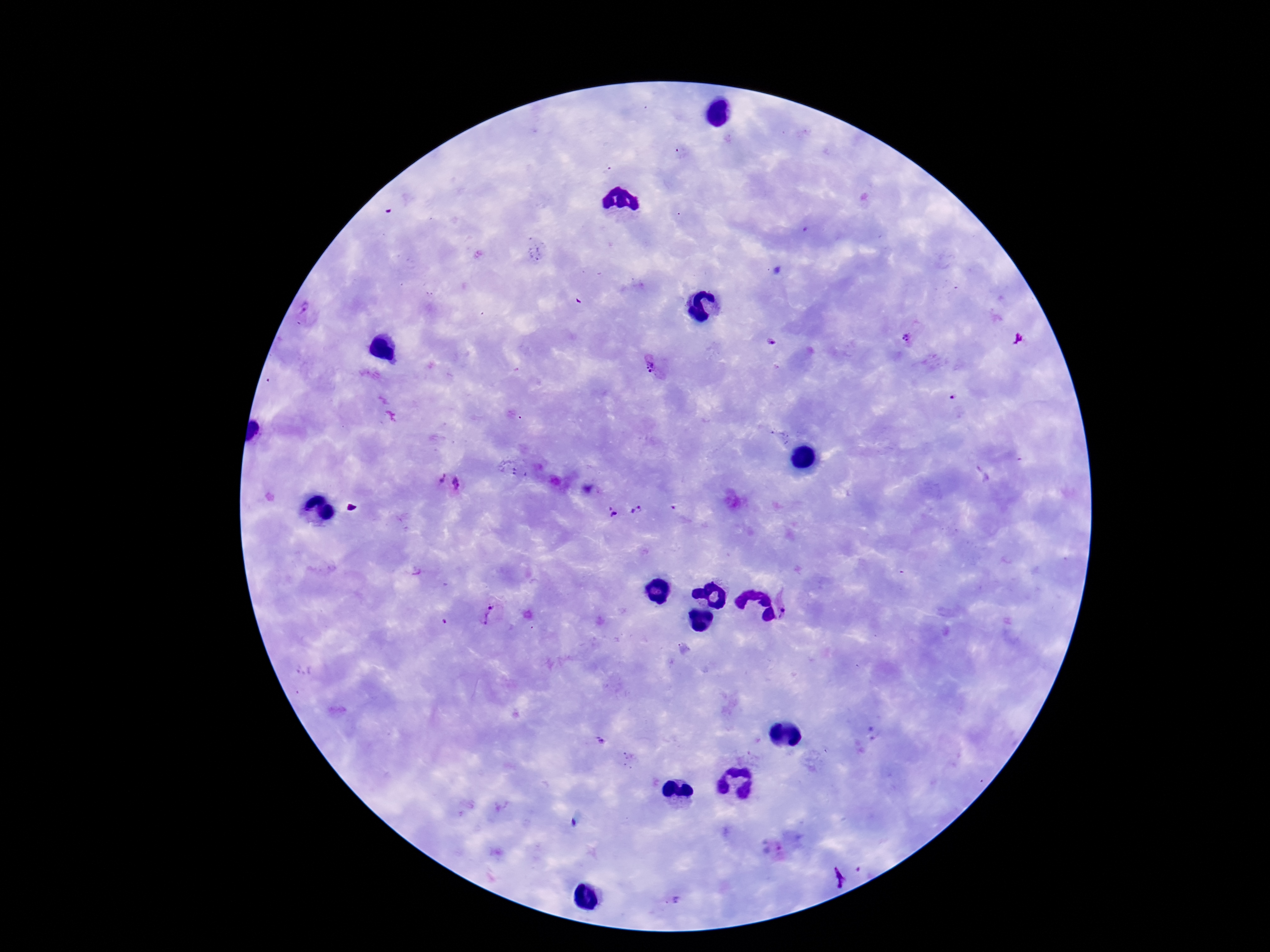
patient_malaria_status: infected
stain: Giemsa
image_size: 1270×952 pixels
preparation: thick peripheral-blood smear
plasmodium_parasite_locations: 'approximate centers as (x, y) in pixels: (305, 309), (907, 338), (771, 342), (649, 366), (952, 397), (781, 436), (438, 478), (458, 483), (610, 508), (674, 508), (637, 510), (614, 514), (790, 607), (490, 608), (486, 619), (444, 622), (304, 670), (601, 740), (777, 849), (839, 874), (676, 900)'
capture: smartphone camera through the microscope eyepiece
magnification: 100x
field_of_view: single